Classify this cell by malaria status.
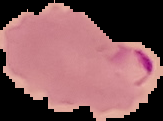
Parasitized.

Summary:
  - Preparation: thin blood film
  - Image size: 163×121 pixels
  - Image type: segmented cell region with the area outside set to black